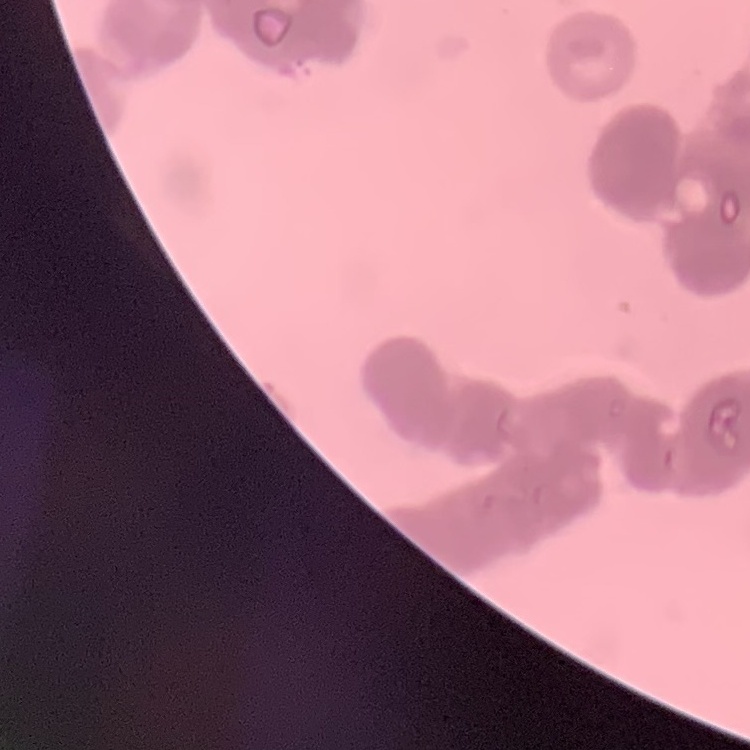

erythrocyte morphology = rouleaux formation
stain = Field's or Giemsa
preparation = thin peripheral smear
image type = one tile cut from a larger photomicrograph